Identify the blood parasite species.
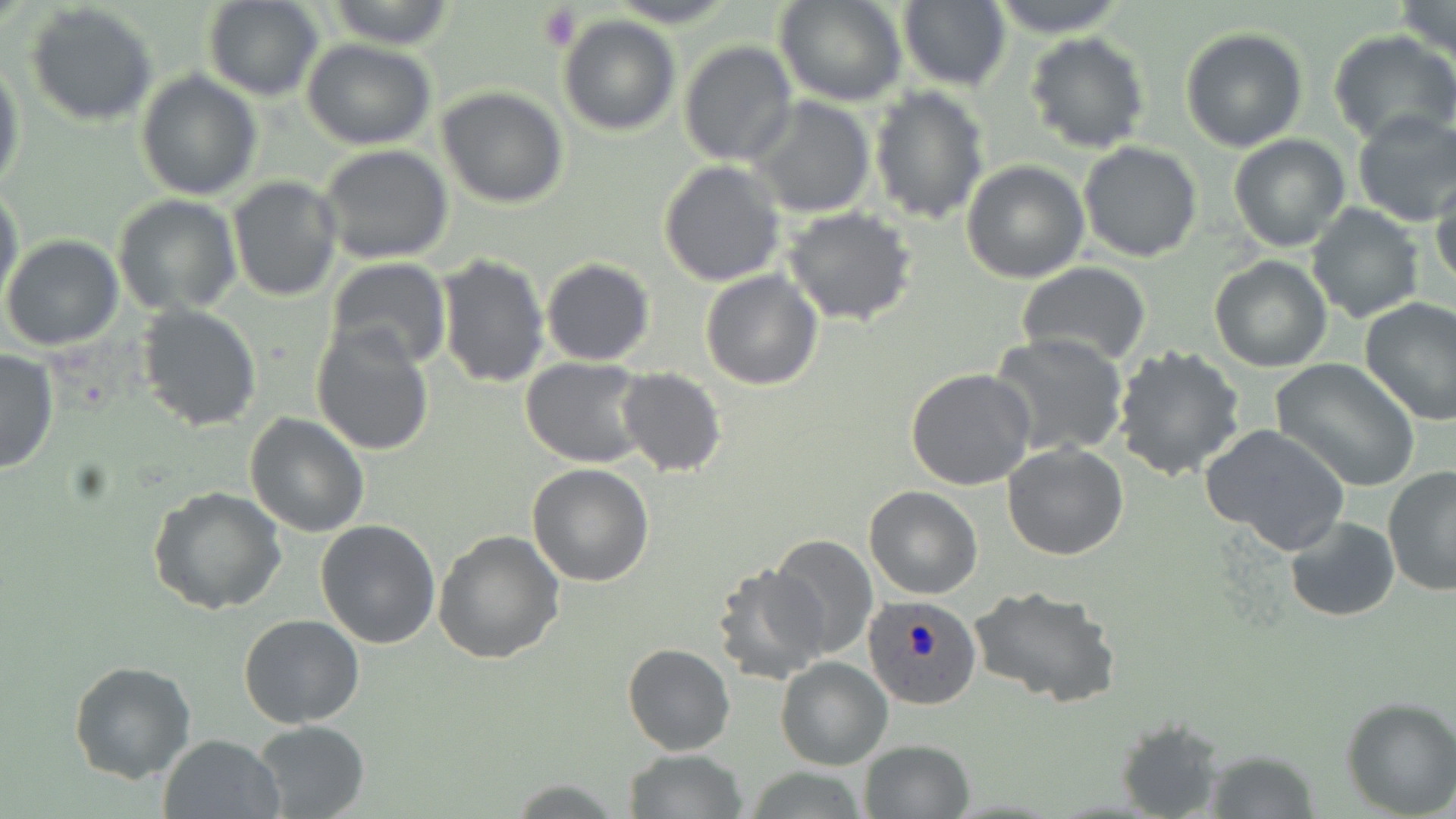
Plasmodium ovale.

uninfected red blood cell locations = approximate bounding boxes as named x1/y1/x2/y2 corners in pixels: (x1=607, y1=0, x2=740, y2=27), (x1=775, y1=0, x2=909, y2=107), (x1=898, y1=0, x2=1013, y2=92), (x1=984, y1=0, x2=1134, y2=36), (x1=203, y1=1, x2=324, y2=101), (x1=324, y1=1, x2=458, y2=49), (x1=1393, y1=2, x2=1455, y2=60), (x1=26, y1=6, x2=155, y2=128), (x1=557, y1=14, x2=681, y2=135), (x1=1180, y1=26, x2=1310, y2=152), (x1=1328, y1=31, x2=1456, y2=148), (x1=1023, y1=32, x2=1151, y2=153), (x1=301, y1=39, x2=438, y2=149), (x1=679, y1=42, x2=797, y2=166), (x1=0, y1=61, x2=24, y2=197), (x1=135, y1=71, x2=262, y2=200), (x1=868, y1=84, x2=990, y2=225), (x1=436, y1=86, x2=569, y2=208), (x1=747, y1=95, x2=877, y2=219), (x1=1350, y1=109, x2=1456, y2=226), (x1=1229, y1=133, x2=1351, y2=252), (x1=1078, y1=140, x2=1203, y2=261), (x1=319, y1=145, x2=454, y2=264), (x1=961, y1=159, x2=1090, y2=283), (x1=658, y1=160, x2=786, y2=286), (x1=1430, y1=172, x2=1456, y2=290), (x1=227, y1=177, x2=342, y2=301), (x1=0, y1=184, x2=23, y2=309), (x1=112, y1=194, x2=242, y2=315), (x1=1305, y1=202, x2=1426, y2=323), (x1=784, y1=206, x2=918, y2=328), (x1=1, y1=234, x2=123, y2=350), (x1=434, y1=252, x2=550, y2=389), (x1=1208, y1=256, x2=1332, y2=372), (x1=326, y1=258, x2=451, y2=372), (x1=541, y1=259, x2=654, y2=365), (x1=1017, y1=261, x2=1151, y2=366), (x1=699, y1=270, x2=823, y2=391), (x1=1358, y1=297, x2=1456, y2=425), (x1=137, y1=304, x2=263, y2=432), (x1=311, y1=324, x2=435, y2=455), (x1=988, y1=332, x2=1129, y2=457), (x1=1111, y1=345, x2=1245, y2=482), (x1=0, y1=349, x2=59, y2=474), (x1=521, y1=358, x2=653, y2=468), (x1=1271, y1=358, x2=1421, y2=493), (x1=616, y1=368, x2=727, y2=477), (x1=905, y1=368, x2=1037, y2=491), (x1=244, y1=412, x2=370, y2=536), (x1=1200, y1=423, x2=1351, y2=557), (x1=1002, y1=443, x2=1129, y2=561), (x1=527, y1=465, x2=655, y2=586), (x1=1382, y1=466, x2=1456, y2=597), (x1=147, y1=486, x2=287, y2=614), (x1=864, y1=486, x2=984, y2=599), (x1=1284, y1=517, x2=1400, y2=621), (x1=315, y1=519, x2=440, y2=649), (x1=433, y1=529, x2=566, y2=666), (x1=770, y1=536, x2=877, y2=661), (x1=711, y1=564, x2=832, y2=687), (x1=969, y1=586, x2=1119, y2=708), (x1=238, y1=614, x2=365, y2=729), (x1=622, y1=643, x2=735, y2=756), (x1=774, y1=657, x2=892, y2=770), (x1=67, y1=661, x2=196, y2=783), (x1=1341, y1=696, x2=1456, y2=817), (x1=1115, y1=716, x2=1227, y2=819), (x1=251, y1=720, x2=372, y2=818), (x1=157, y1=732, x2=286, y2=818), (x1=858, y1=739, x2=976, y2=819), (x1=626, y1=747, x2=745, y2=817), (x1=1204, y1=748, x2=1320, y2=818), (x1=743, y1=766, x2=873, y2=818), (x1=505, y1=778, x2=626, y2=815)
field of view = one of a larger specimen
magnification = 1000x
preparation = thin blood smear
modality = optical microscopy
platelet locations = approximate bounding boxes as named x1/y1/x2/y2 corners in pixels: (x1=537, y1=5, x2=581, y2=53)
Plasmodium ovale-infected red blood cell locations = approximate bounding boxes as named x1/y1/x2/y2 corners in pixels: (x1=863, y1=595, x2=983, y2=709)
stain = May-Grünwald-Giemsa
image size = 1456×819 pixels